Assess the morphology of the red blood cells.
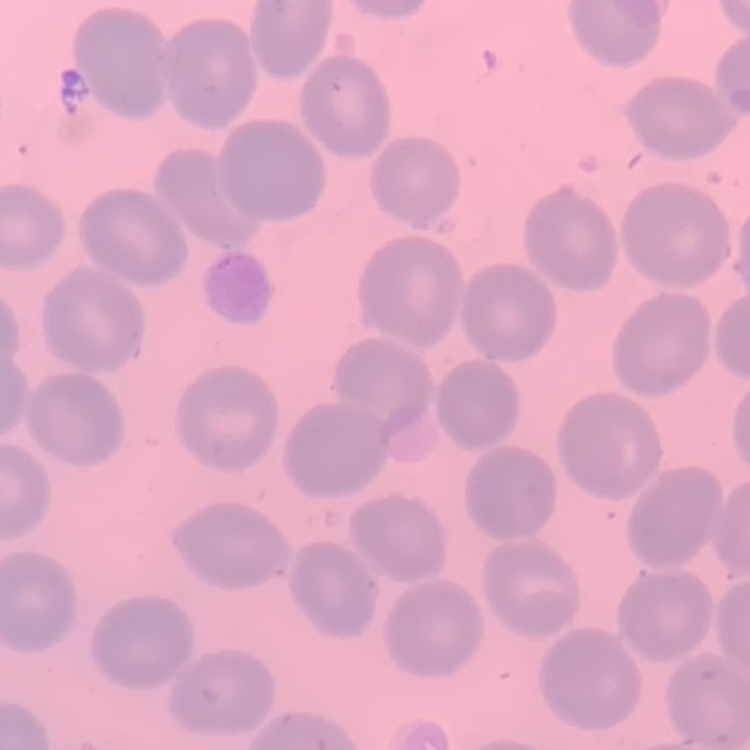

No rouleaux formation.

Field's or Giemsa stain. Thin blood film. One tile cut from a larger photomicrograph.